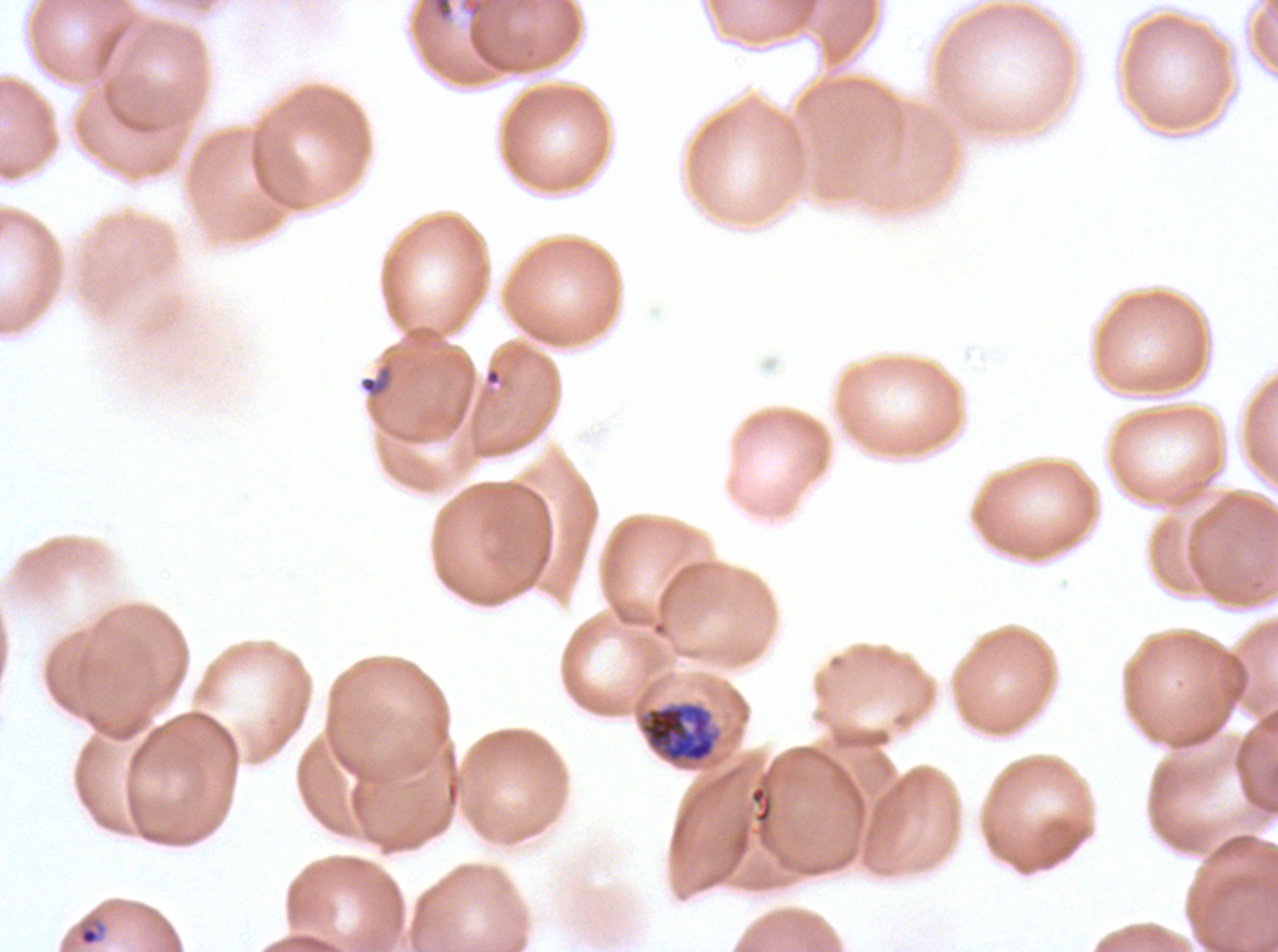

{
  "life_cycle_stages_observed": "ring, early schizont",
  "stain": "Giemsa",
  "field_of_view": "sub-image separated from a larger composite",
  "preparation": "thin blood smear",
  "ring_locations": "approximate bounding boxes as [x1, y1, x2, y2] in pixels: [78, 921, 107, 947]",
  "debris_locations": "approximate bounding boxes as [x1, y1, x2, y2] in pixels: [430, 0, 454, 21], [358, 364, 395, 398]",
  "specimen": "P. falciparum cultured ex vivo for 24 to 48 hours, from a patient in The Gambia",
  "image_size": "1278×952 pixels",
  "early_schizont_locations": "approximate bounding boxes as [x1, y1, x2, y2] in pixels: [640, 702, 716, 763]"
}